Assess this cell for malaria.
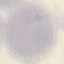
It is uninfected.

Acquired by smartphone through the microscope eyepiece. Cell patch, automatically extracted from a larger field of view and resized to 64 × 64 pixels. Giemsa stain. Thin smear of blood.